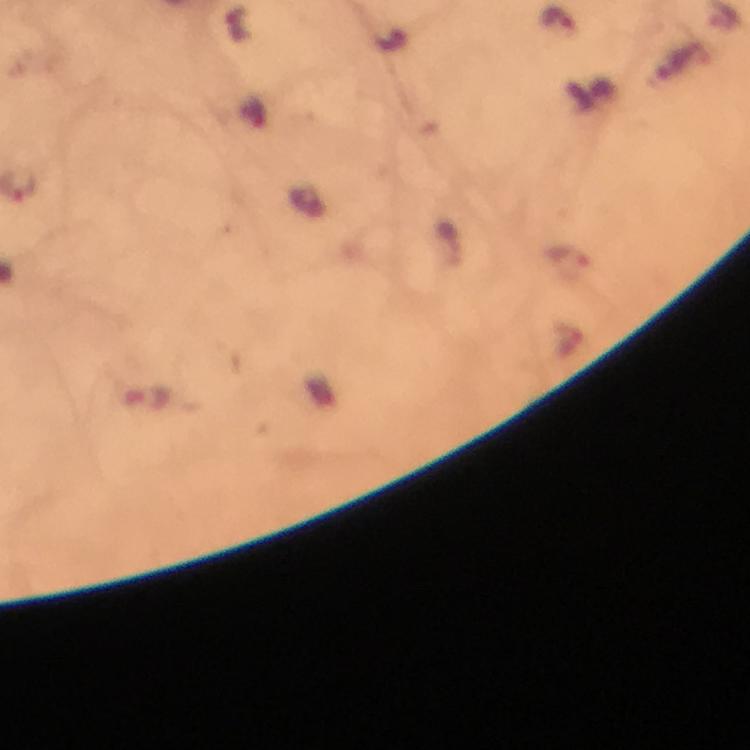

magnification = 100x
context = from a malaria diagnostic workup
image size = 750×750 pixels
stain = Giemsa
Plasmodium parasite locations = approximate centers as {x, y} in pixels: {557, 19}
capture = smartphone camera through the microscope
cropped from = one field of view
immersion oil = used
preparation = thick blood smear